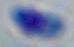 Micrograph. Captured at 1000x magnification. Toxoplasma gondii is shown.